Outline platelets.
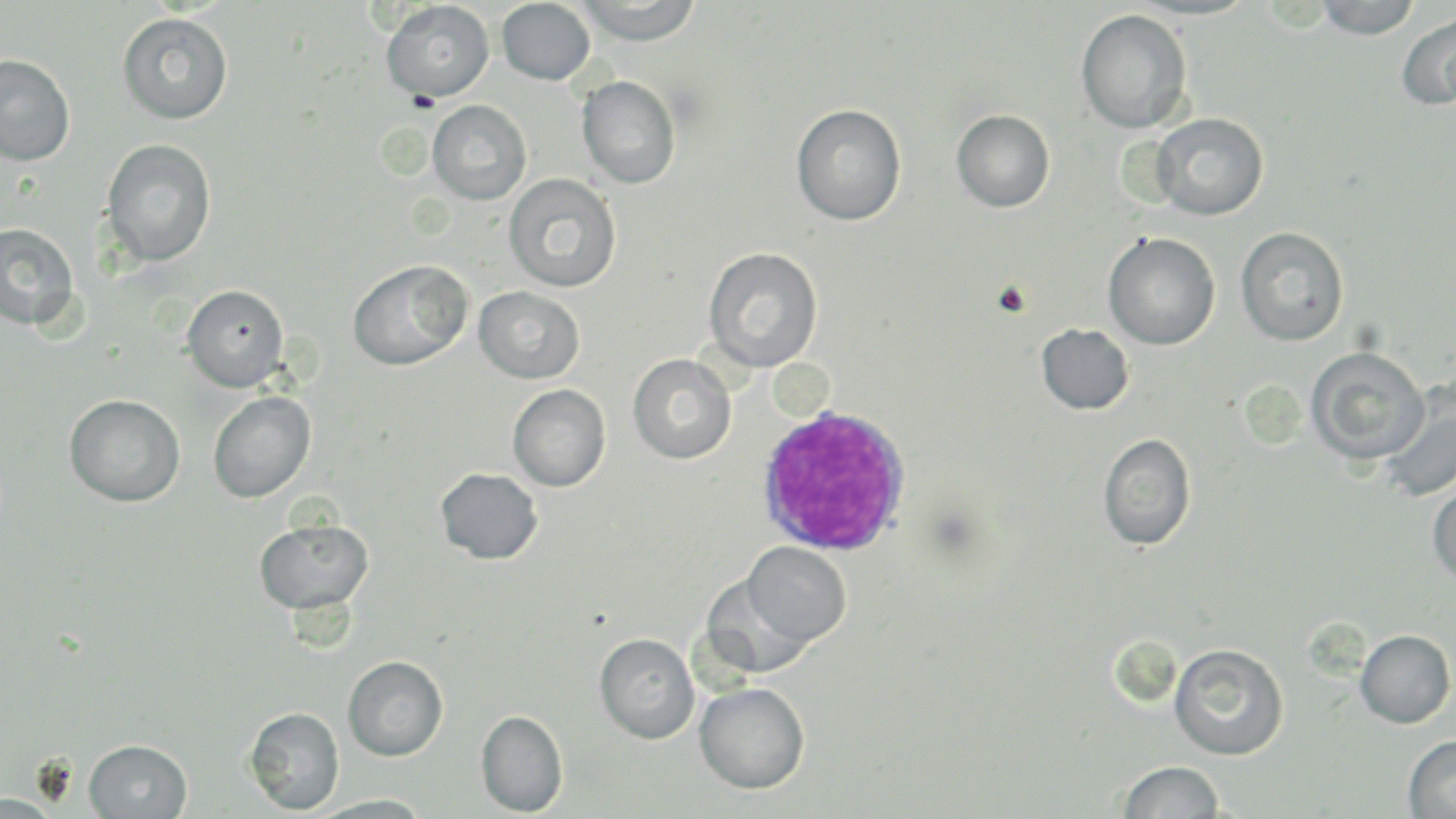
Approximate bounding boxes as (x1, y1, x2, y2) in pixels.
Platelets: (992, 279, 1033, 318).

Uninfected red blood cell locations: (576, 0, 703, 45), (1127, 0, 1257, 20), (1315, 0, 1421, 39), (381, 1, 495, 101), (496, 1, 596, 84), (1076, 9, 1193, 134), (1397, 11, 1456, 111), (118, 13, 233, 125), (0, 55, 75, 165), (577, 76, 681, 189), (428, 100, 531, 205), (791, 104, 907, 226), (951, 109, 1055, 212), (1150, 112, 1268, 220), (101, 139, 217, 268), (504, 173, 622, 293), (0, 222, 80, 330), (1235, 226, 1349, 346), (1102, 231, 1221, 350), (703, 246, 823, 372), (348, 260, 473, 370), (182, 284, 289, 392), (473, 285, 584, 384), (1036, 324, 1135, 415), (1306, 347, 1429, 465), (628, 354, 736, 464), (507, 384, 611, 491), (1378, 386, 1456, 503), (207, 391, 316, 503), (64, 394, 186, 507), (1098, 433, 1196, 551), (435, 468, 542, 564), (1427, 477, 1456, 585), (254, 518, 374, 614), (743, 542, 851, 646), (702, 574, 814, 678), (1355, 629, 1455, 728), (594, 633, 700, 744), (1168, 642, 1289, 760), (343, 656, 448, 761), (695, 682, 810, 794), (245, 707, 344, 815), (476, 709, 568, 816), (1403, 734, 1456, 818), (85, 739, 193, 818), (1118, 761, 1225, 818), (0, 794, 62, 817), (308, 794, 434, 817). White blood cell locations: (753, 403, 913, 556). Slide-level diagnosis: Plasmodium ovale. May-Grünwald-Giemsa-stained preparation. Image is 1456×819 pixels. Thin blood film. One field of a larger specimen. Captured at 1000x magnification. Light microscopy.